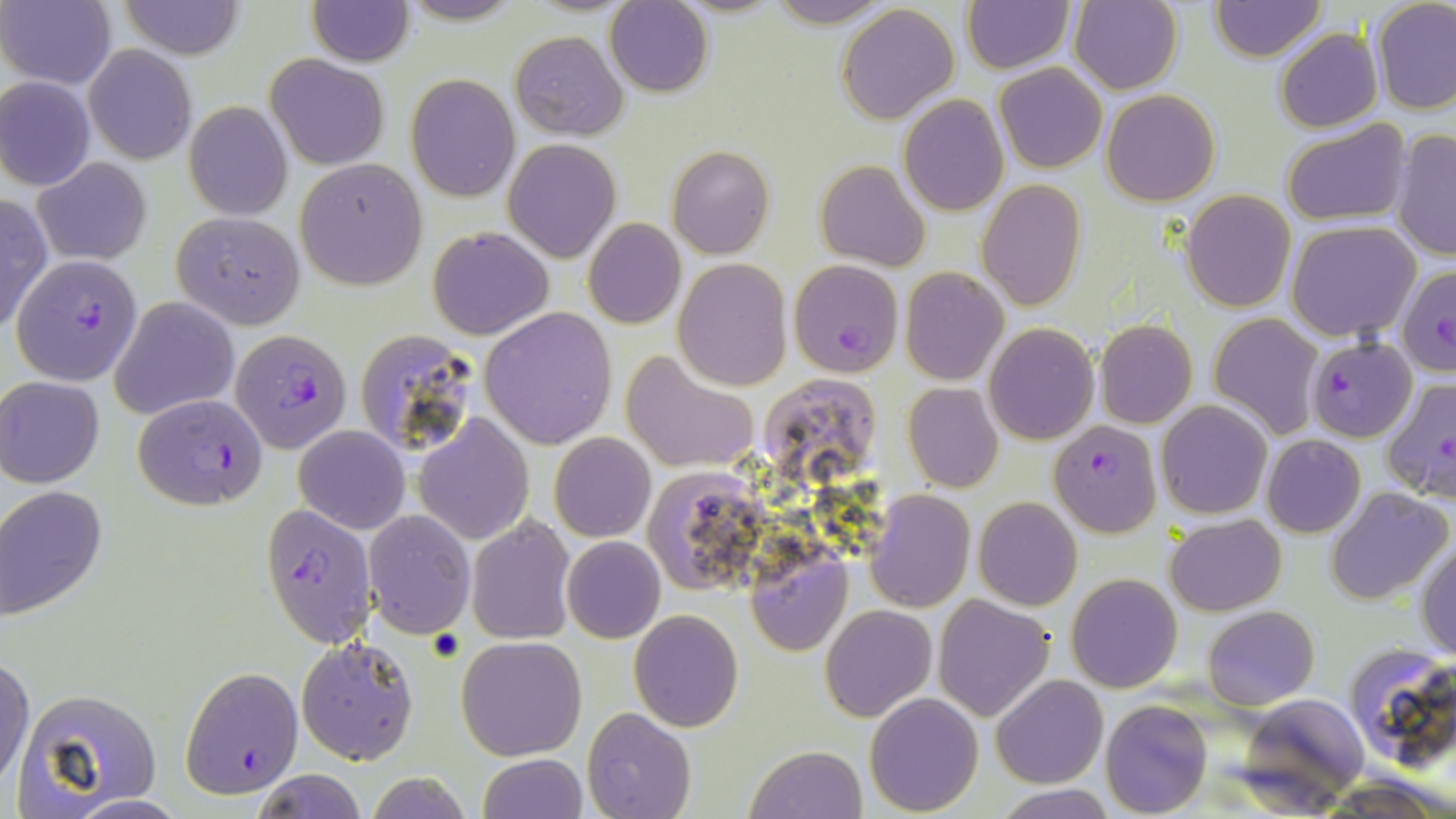
Approximate bounding boxes as [x1, y1, x2, y2] in pixels. Plasmodium falciparum-infected red blood cell locations: [11, 254, 144, 385], [788, 259, 904, 378], [1395, 264, 1456, 378], [1306, 337, 1417, 441], [247, 341, 361, 472], [1381, 377, 1456, 506], [132, 393, 267, 509], [1048, 421, 1162, 537], [181, 667, 303, 798]. Uninfected red blood cell locations: [1, 0, 115, 90], [763, 0, 900, 26], [1069, 0, 1182, 94], [118, 1, 245, 59], [306, 1, 415, 67], [961, 1, 1074, 74], [1209, 1, 1326, 62], [606, 2, 712, 96], [1370, 2, 1456, 114], [837, 5, 960, 125], [1274, 28, 1383, 133], [509, 31, 627, 139], [83, 44, 196, 164], [266, 55, 388, 170], [994, 63, 1107, 173], [405, 73, 519, 203], [0, 76, 96, 191], [1101, 90, 1220, 206], [899, 96, 1010, 216], [183, 100, 295, 220], [1280, 121, 1410, 227], [1390, 128, 1455, 263], [503, 139, 620, 262], [667, 146, 774, 258], [33, 157, 151, 266], [295, 160, 427, 290], [815, 160, 930, 273], [975, 181, 1085, 309], [1181, 189, 1295, 311], [0, 191, 51, 338], [172, 211, 305, 328], [582, 219, 685, 329], [1287, 221, 1422, 339], [429, 227, 553, 340], [673, 258, 793, 389], [900, 267, 1008, 385], [109, 297, 238, 420], [481, 310, 617, 449], [1209, 313, 1323, 439], [1095, 320, 1197, 428], [985, 324, 1099, 445], [620, 349, 761, 474], [1, 375, 107, 488], [763, 376, 887, 489], [901, 382, 1003, 493], [1155, 401, 1272, 519], [415, 415, 534, 544], [295, 425, 409, 533], [550, 433, 655, 542], [1262, 435, 1365, 538], [646, 469, 765, 586], [1324, 486, 1452, 605], [0, 487, 108, 622], [865, 491, 975, 611], [974, 497, 1082, 610], [260, 503, 377, 649], [363, 511, 475, 638], [467, 514, 576, 644], [1166, 515, 1285, 615], [562, 536, 666, 644], [1417, 538, 1456, 662], [746, 550, 849, 656], [1066, 573, 1182, 692], [932, 595, 1055, 721], [819, 604, 937, 722], [1203, 606, 1319, 710], [629, 610, 743, 731], [296, 635, 419, 767], [455, 636, 585, 760], [1342, 644, 1456, 775], [1, 656, 34, 792], [992, 676, 1108, 788], [15, 688, 162, 810], [864, 693, 983, 814], [1236, 693, 1368, 806], [1101, 699, 1213, 817], [582, 708, 697, 819], [743, 745, 869, 819], [477, 753, 587, 819], [252, 771, 368, 818], [992, 783, 1118, 819]. Slide-level diagnosis: Plasmodium falciparum. Image is 1456×819 pixels. One field of a larger specimen. 1000x magnification. Thin blood smear. May-Grünwald-Giemsa-stained preparation. Light microscopy.